Point out each leukocyte.
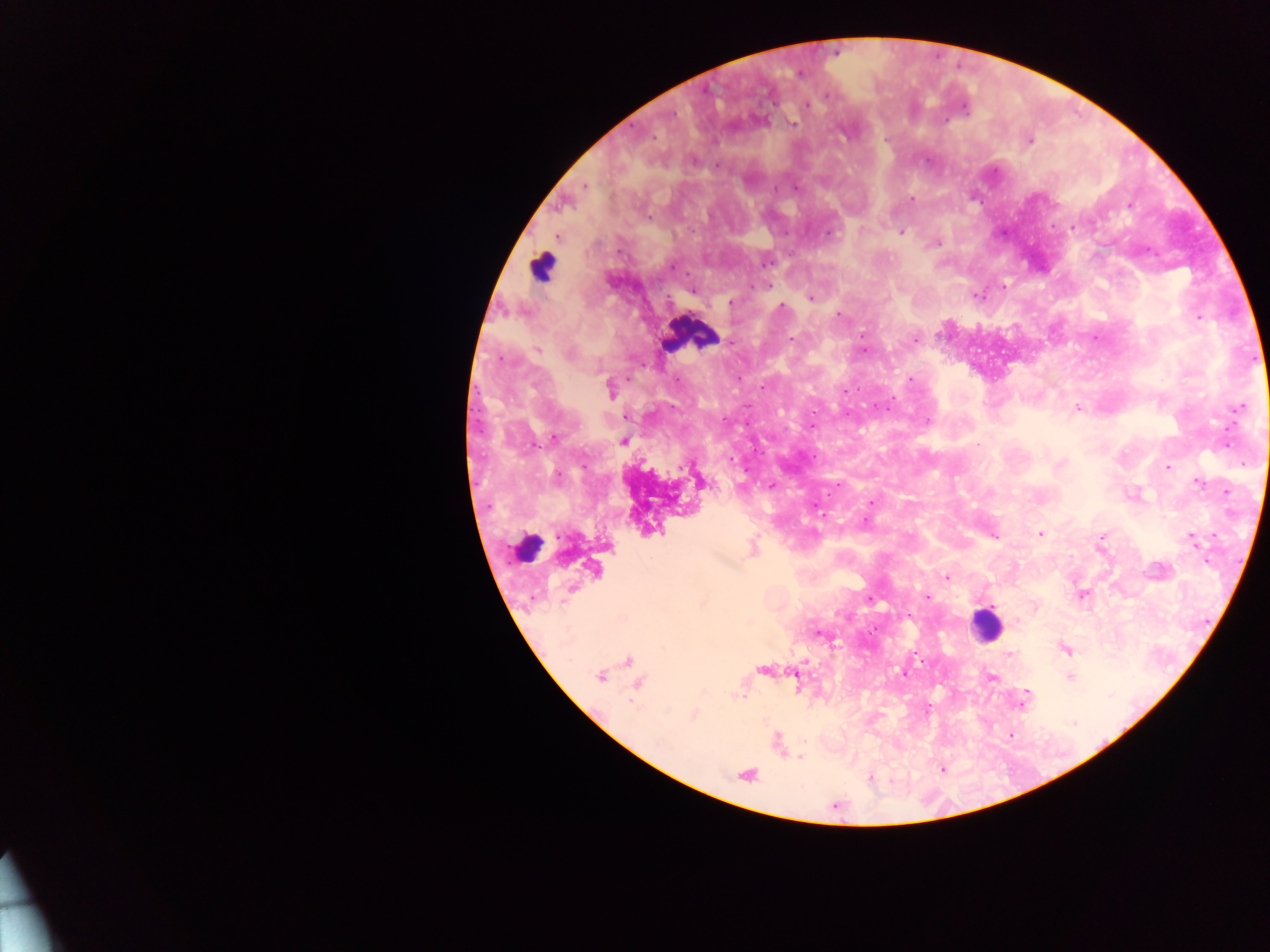

Approximate centers as (x, y) in pixels.
Leukocytes: (541, 267), (691, 334), (531, 551), (986, 624).

country = Ghana
Plasmodium parasite locations = approximate centers as (x, y) in pixels: (800, 73), (827, 95), (807, 105), (965, 110), (793, 124), (886, 139), (1029, 140), (926, 160), (694, 161), (717, 165), (586, 186), (775, 189), (911, 199), (650, 217), (1072, 227), (902, 232), (827, 235), (937, 244), (768, 263), (672, 267), (767, 286), (1003, 286), (755, 287), (692, 291), (976, 295), (810, 298), (730, 303), (782, 306), (838, 315), (1199, 318), (791, 339), (915, 339), (731, 343), (538, 350), (864, 350), (568, 354), (502, 359), (739, 378), (911, 379), (676, 380), (761, 387), (610, 388), (844, 391), (883, 407), (1077, 408), (1238, 408), (847, 413), (626, 417), (723, 420), (927, 420), (811, 426), (555, 436), (623, 441), (1226, 444), (977, 445), (730, 459), (1168, 467), (746, 471), (557, 476), (1198, 484), (838, 485), (771, 486), (871, 502), (1041, 533), (1101, 536), (1193, 539), (651, 559), (1207, 561), (946, 577), (1082, 595), (926, 596), (870, 600), (1017, 621), (874, 630), (819, 635), (1066, 651), (903, 673), (599, 676), (991, 676), (1070, 676), (1027, 693), (743, 697), (1025, 698), (1022, 704), (693, 715), (1073, 722), (1012, 736), (800, 757)
image size = 1270×952 pixels
field of view = single
capture = mobile-phone photograph through a microscope
preparation = thick blood smear